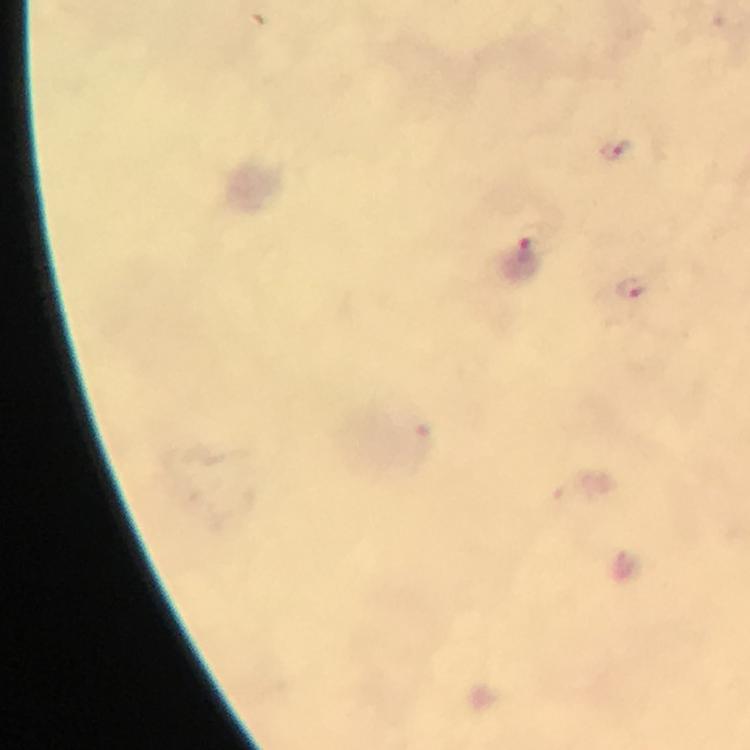
Approximate object centers, in pixels from the top-left corner. Plasmodium parasite locations: (x=621, y=151), (x=530, y=248), (x=632, y=286). Immersion oil was used. Image is 750×750 pixels. Photographed through the microscope with a smartphone camera. A crop from one field of view. Thick blood film. From a diagnostic examination for malaria. 100x magnification. Giemsa stain.